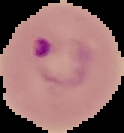

Summary:
  - Preparation: thin blood film
  - Image size: 124×133 pixels
  - Image type: cell region segmented out of the field of view; surrounding area masked to black
  - Malaria status: parasitized